Classify this cell by malaria status.
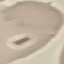
It is uninfected.

Summary:
  - Image type: automatically extracted cell patch, resized to 64 × 64 pixels
  - Preparation: thin smear
  - Stain: Giemsa
  - Capture: smartphone through the microscope eyepiece